Outline each blood parasite and name the species.
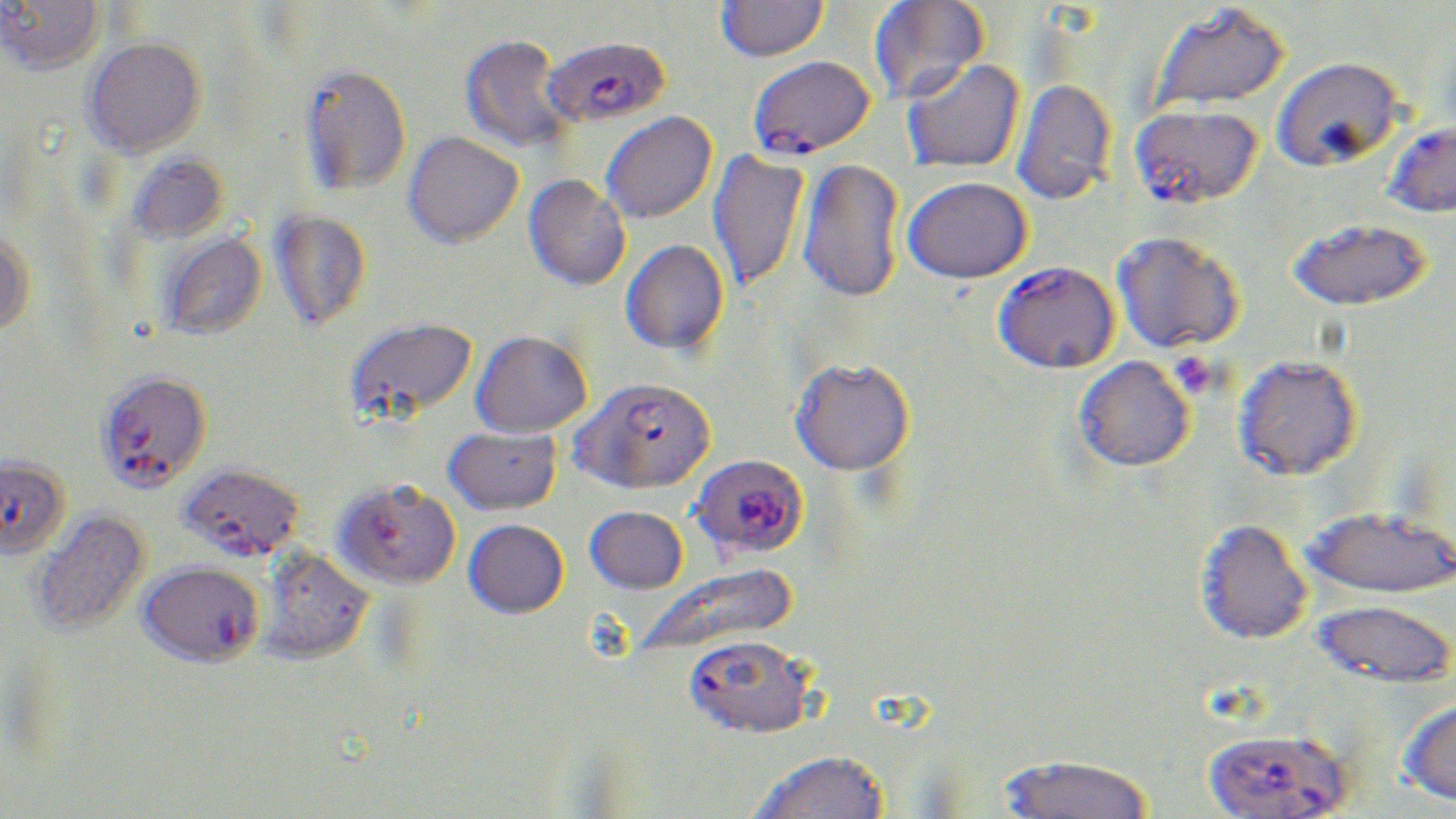
Approximate bounding boxes as [x1, y1, x2, y2] in pixels.
Plasmodium falciparum-infected red blood cells: [542, 35, 670, 127], [748, 55, 876, 158], [1129, 103, 1262, 208], [1380, 119, 1456, 218], [993, 260, 1119, 373], [94, 370, 212, 493], [573, 376, 716, 493], [0, 455, 70, 560], [694, 457, 806, 552], [178, 463, 305, 561], [334, 477, 461, 589], [138, 560, 264, 667], [683, 635, 816, 741], [1200, 726, 1354, 818].
No Plasmodium ovale, Plasmodium malariae, Plasmodium vivax, Babesia divergens, or Trypanosoma brucei observed.

Platelet locations: [1173, 354, 1207, 400]. Uninfected red blood cell locations: [1, 0, 105, 73], [716, 0, 829, 62], [868, 1, 988, 104], [1148, 2, 1290, 114], [460, 34, 570, 154], [83, 37, 206, 158], [1270, 55, 1402, 171], [901, 58, 1025, 174], [299, 63, 412, 195], [1012, 78, 1116, 206], [600, 111, 716, 224], [403, 131, 523, 248], [706, 150, 810, 293], [127, 152, 229, 245], [797, 157, 906, 304], [523, 174, 631, 291], [903, 176, 1032, 283], [270, 209, 371, 331], [1288, 218, 1433, 310], [0, 230, 36, 336], [1111, 230, 1243, 354], [160, 231, 267, 340], [620, 238, 729, 356], [344, 316, 477, 424], [471, 329, 592, 437], [1232, 354, 1362, 480], [1073, 356, 1195, 472], [790, 357, 915, 475], [443, 425, 561, 516], [1302, 504, 1456, 600], [585, 505, 687, 594], [30, 508, 151, 636], [464, 518, 568, 618], [1194, 518, 1313, 645], [257, 547, 374, 664], [637, 566, 795, 658], [1313, 599, 1455, 689], [1397, 696, 1456, 806], [747, 751, 889, 819], [997, 753, 1154, 819]. Slide-level diagnosis: Plasmodium falciparum. One field of a larger specimen. May-Grünwald-Giemsa stain. 1000x magnification. Thin blood smear. Optical microscopy. Image is 1456×819 pixels.